Locate every blood parasite and identify its species.
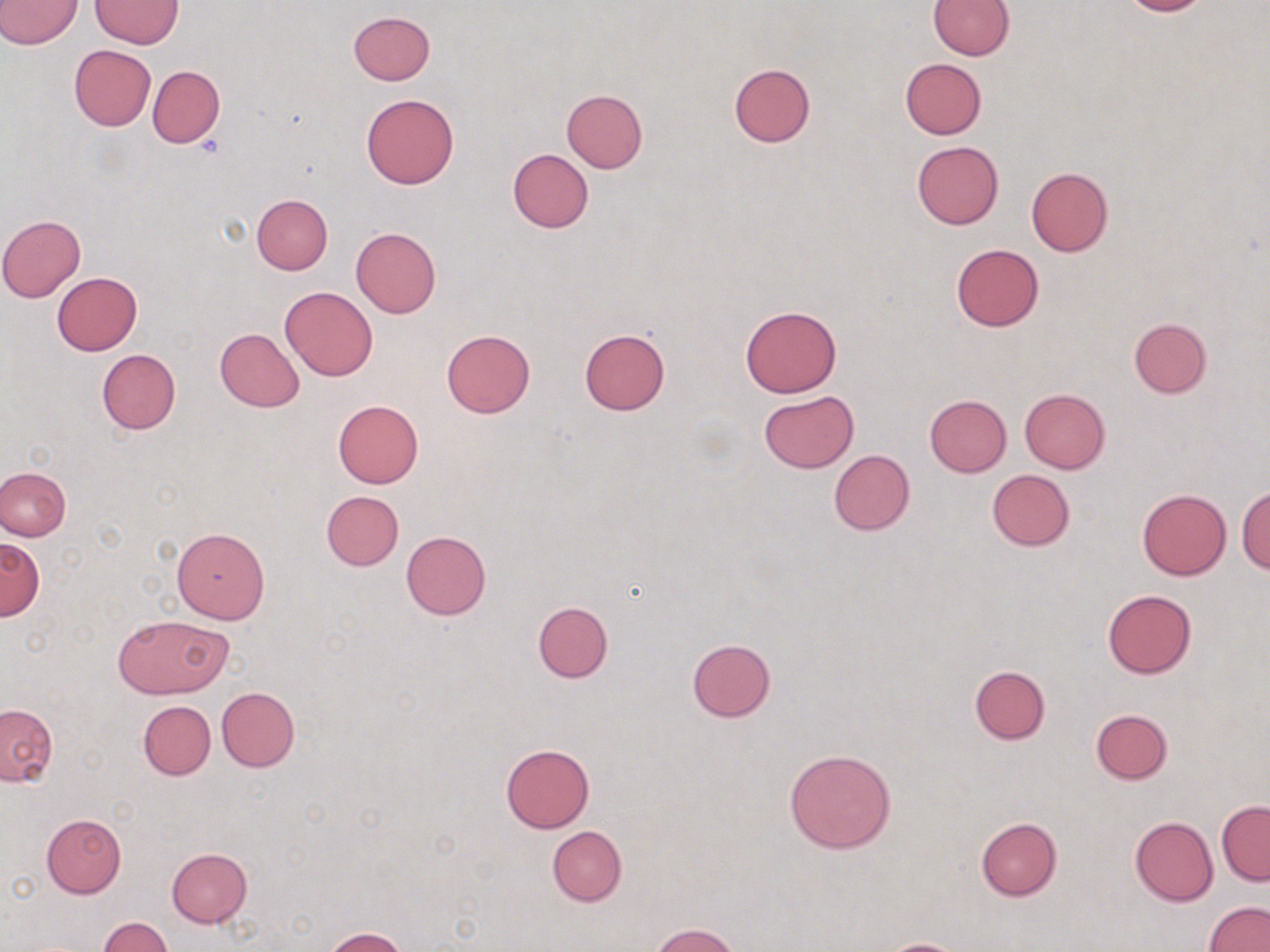
No blood parasites seen.

slide-level diagnosis = no evidence of blood parasites
uninfected red blood cell locations = approximate bounding boxes as [x1, y1, x2, y2] in pixels: [0, 0, 81, 49], [91, 0, 184, 48], [927, 0, 1014, 60], [1116, 0, 1213, 17], [349, 11, 434, 86], [68, 44, 156, 131], [899, 58, 985, 140], [729, 63, 815, 148], [148, 66, 225, 148], [563, 89, 647, 174], [360, 92, 459, 188], [911, 141, 1003, 229], [508, 149, 593, 233], [1025, 166, 1112, 257], [251, 193, 333, 274], [0, 215, 85, 302], [351, 227, 441, 317], [952, 243, 1044, 331], [52, 272, 142, 355], [280, 286, 377, 382], [740, 304, 843, 398], [1128, 317, 1213, 399], [214, 327, 305, 412], [577, 329, 670, 415], [441, 330, 535, 418], [96, 349, 180, 434], [1019, 388, 1110, 473], [758, 392, 858, 472], [923, 395, 1012, 477], [332, 399, 424, 487], [829, 450, 915, 535], [0, 467, 71, 540], [987, 469, 1074, 550], [1237, 486, 1270, 573], [1136, 489, 1232, 580], [320, 490, 403, 571], [171, 526, 270, 623], [401, 530, 491, 621], [0, 538, 43, 620], [1102, 589, 1196, 678], [533, 600, 614, 684], [115, 614, 230, 699], [687, 638, 776, 721], [969, 664, 1051, 745], [216, 687, 299, 771], [138, 701, 216, 780], [0, 704, 57, 786], [1090, 708, 1173, 784], [500, 744, 595, 833], [785, 748, 896, 853], [1217, 801, 1270, 885], [41, 813, 126, 896], [1130, 815, 1218, 906], [976, 817, 1061, 901], [548, 826, 627, 907], [167, 848, 252, 927], [1202, 901, 1270, 952], [99, 915, 172, 952], [650, 924, 741, 952], [326, 928, 408, 952], [873, 937, 969, 951]
field of view = one of a larger specimen
magnification = 1000x
modality = light microscopy
image size = 1270×952 pixels
preparation = thin blood smear
stain = May-Grünwald-Giemsa